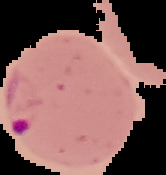

Segmented cell region on a black background. Image is 166×175 pixels. Malaria status: parasitized. From a thin blood film.